Classify this cell by malaria status.
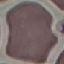
It is uninfected.

Summary:
  - Stain: Giemsa
  - Preparation: thin blood film
  - Capture: smartphone camera at the microscope eyepiece
  - Image type: cell patch, automatically extracted from a larger field of view and resized to 64 × 64 pixels